Give the position of every leukocyte visible.
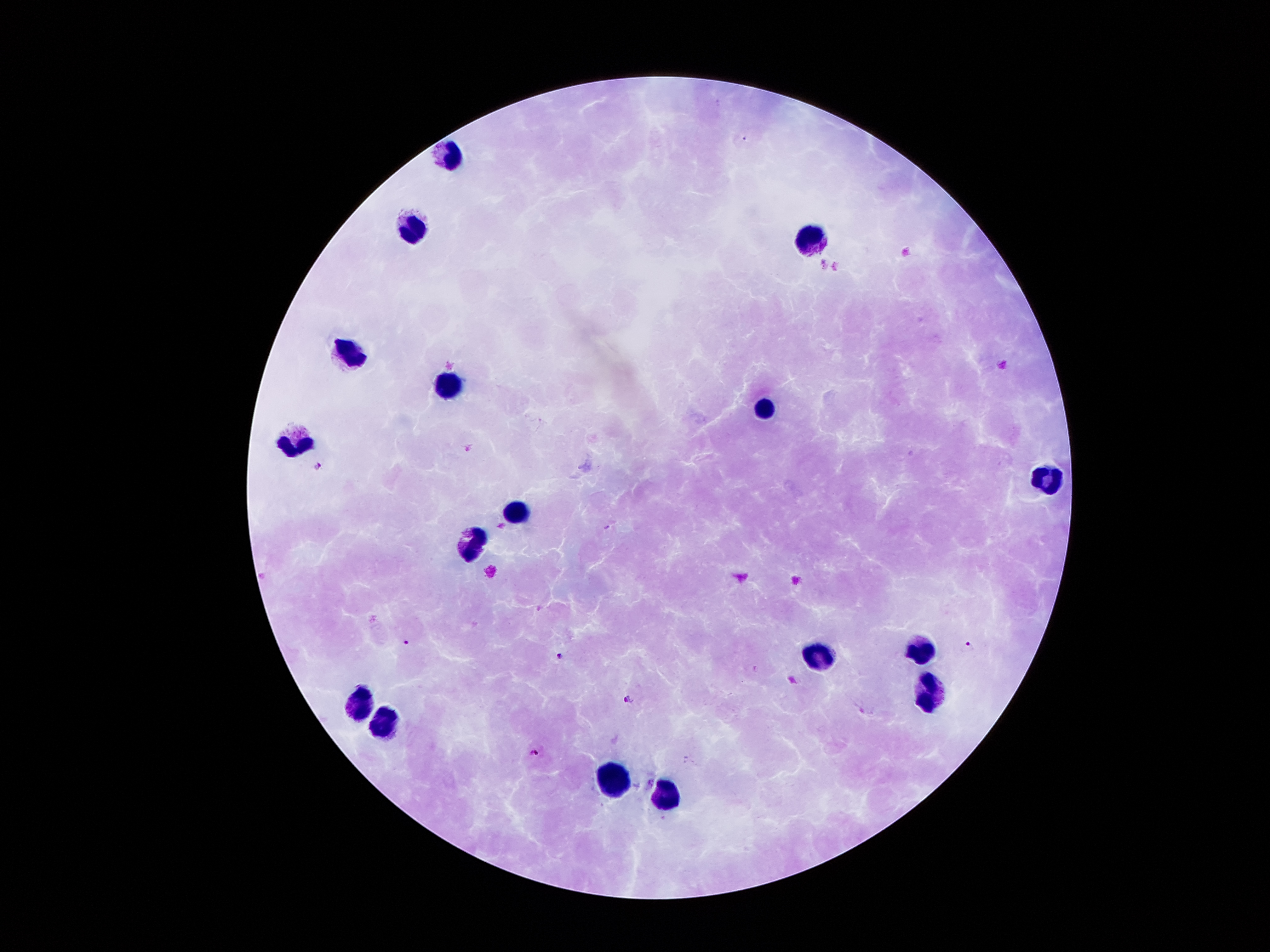

Approximate centers as (x, y) in pixels.
Leukocytes: (453, 159), (414, 228), (810, 239), (350, 356), (447, 387), (763, 407), (294, 439), (1049, 479), (515, 511), (470, 545), (917, 650), (819, 657), (929, 693), (362, 703), (382, 728), (611, 781), (666, 795).

Summary:
  - Malaria parasite locations: (743, 138), (468, 447), (319, 464), (406, 641), (970, 645), (558, 656), (628, 699), (863, 711), (535, 751)
  - Field of view: one from this slide
  - Stain: Giemsa
  - Magnification: 100x
  - Capture: smartphone camera through the microscope eyepiece
  - Image size: 1270×952 pixels
  - Patient malaria status: infected with Plasmodium falciparum
  - Preparation: thick blood film